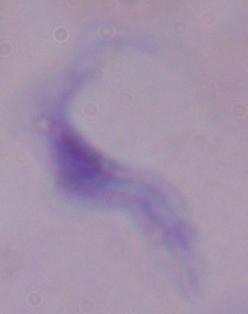

A trypanosome is seen. Captured at 1000x magnification. Photomicrograph.